Locate platelets.
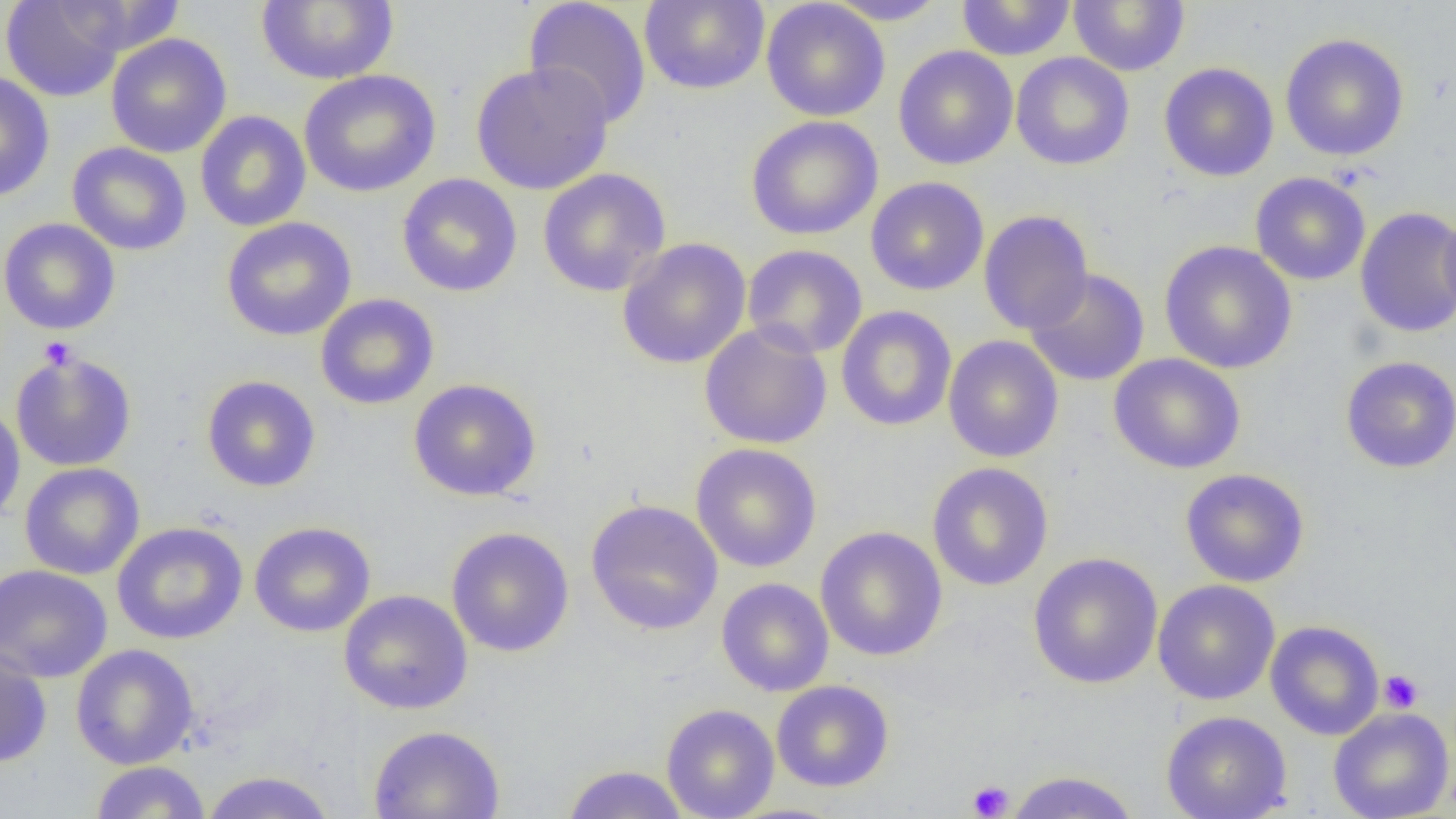

Approximate bounding boxes as [x1, y1, x2, y2] in pixels.
Platelets: [39, 337, 77, 370], [1378, 669, 1424, 713], [967, 780, 1014, 818].

Uninfected red blood cell locations: [1, 0, 127, 102], [524, 0, 651, 129], [823, 0, 950, 25], [1068, 0, 1190, 76], [255, 1, 399, 85], [639, 1, 770, 95], [761, 1, 890, 122], [956, 1, 1076, 61], [52, 2, 189, 54], [105, 33, 232, 158], [1280, 33, 1409, 161], [893, 46, 1019, 170], [1011, 51, 1135, 170], [470, 61, 614, 195], [1158, 62, 1279, 182], [298, 69, 441, 198], [0, 70, 55, 203], [195, 111, 311, 232], [746, 116, 883, 240], [67, 142, 192, 256], [537, 167, 671, 297], [1250, 172, 1371, 286], [396, 174, 523, 297], [865, 176, 989, 296], [1438, 205, 1456, 327], [1355, 206, 1456, 339], [978, 210, 1094, 334], [221, 217, 357, 341], [0, 218, 121, 335], [616, 238, 752, 369], [1159, 241, 1297, 374], [742, 244, 867, 359], [1024, 268, 1150, 386], [315, 293, 440, 410], [835, 305, 957, 432], [699, 323, 833, 450], [943, 335, 1064, 463], [10, 350, 137, 472], [1108, 353, 1246, 474], [1340, 356, 1456, 473], [202, 375, 320, 492], [408, 378, 542, 501], [0, 402, 26, 527], [690, 443, 822, 572], [19, 462, 145, 580], [927, 462, 1054, 591], [1179, 468, 1310, 588], [584, 499, 723, 636], [249, 521, 376, 637], [111, 522, 248, 645], [815, 525, 948, 662], [446, 526, 574, 658], [1027, 552, 1163, 689], [0, 564, 113, 683], [716, 577, 834, 697], [1152, 579, 1280, 705], [339, 590, 473, 714], [1265, 620, 1385, 740], [71, 644, 199, 769], [0, 648, 52, 768], [771, 680, 894, 792], [661, 703, 779, 819], [1328, 707, 1454, 819], [1161, 710, 1293, 819], [368, 725, 505, 819], [90, 761, 212, 818], [560, 764, 691, 818], [200, 770, 336, 819], [1004, 770, 1141, 819]. Slide-level diagnosis: negative for blood parasites. Image is 1456×819 pixels. Optical microscopy. Thin blood film. 1000x magnification. Single field of view.